Locate every Plasmodium parasite.
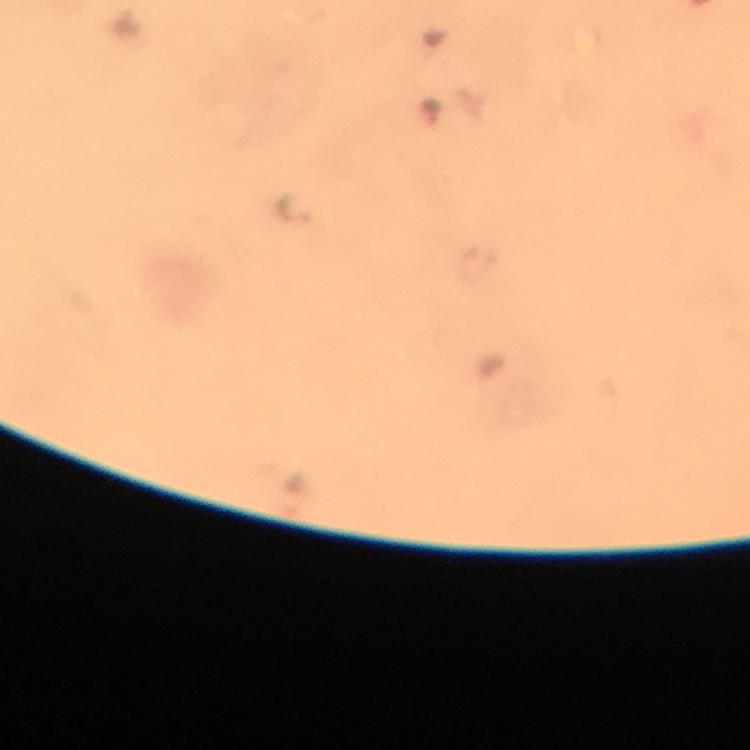
Approximate centers as {x, y} in pixels.
Plasmodium parasites: {433, 112}, {295, 204}.

From a diagnostic examination for malaria. Image is 750×750 pixels. A crop from one field of view. Giemsa stain. Photographed with a smartphone mounted on the microscope. Thick blood film. At 100x magnification. Immersion oil was used.